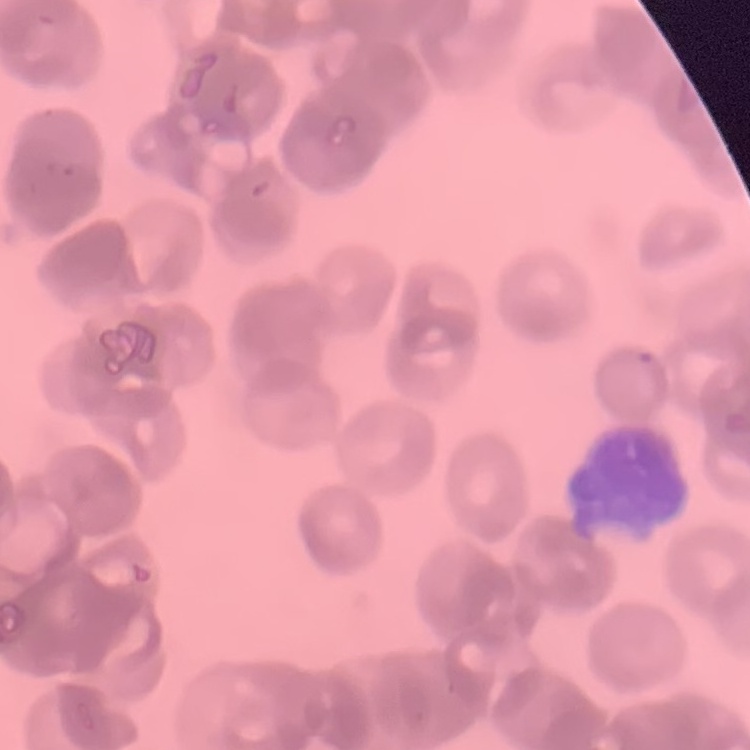

The red blood cells show rouleaux formation. Field's or Giemsa stain. Thin blood film. Square crop of a larger photomicrograph.